Identify the parasite.
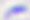
This is Toxoplasma gondii.

Summary:
  - Modality: photomicrograph
  - Magnification: 400x